Report the malaria status.
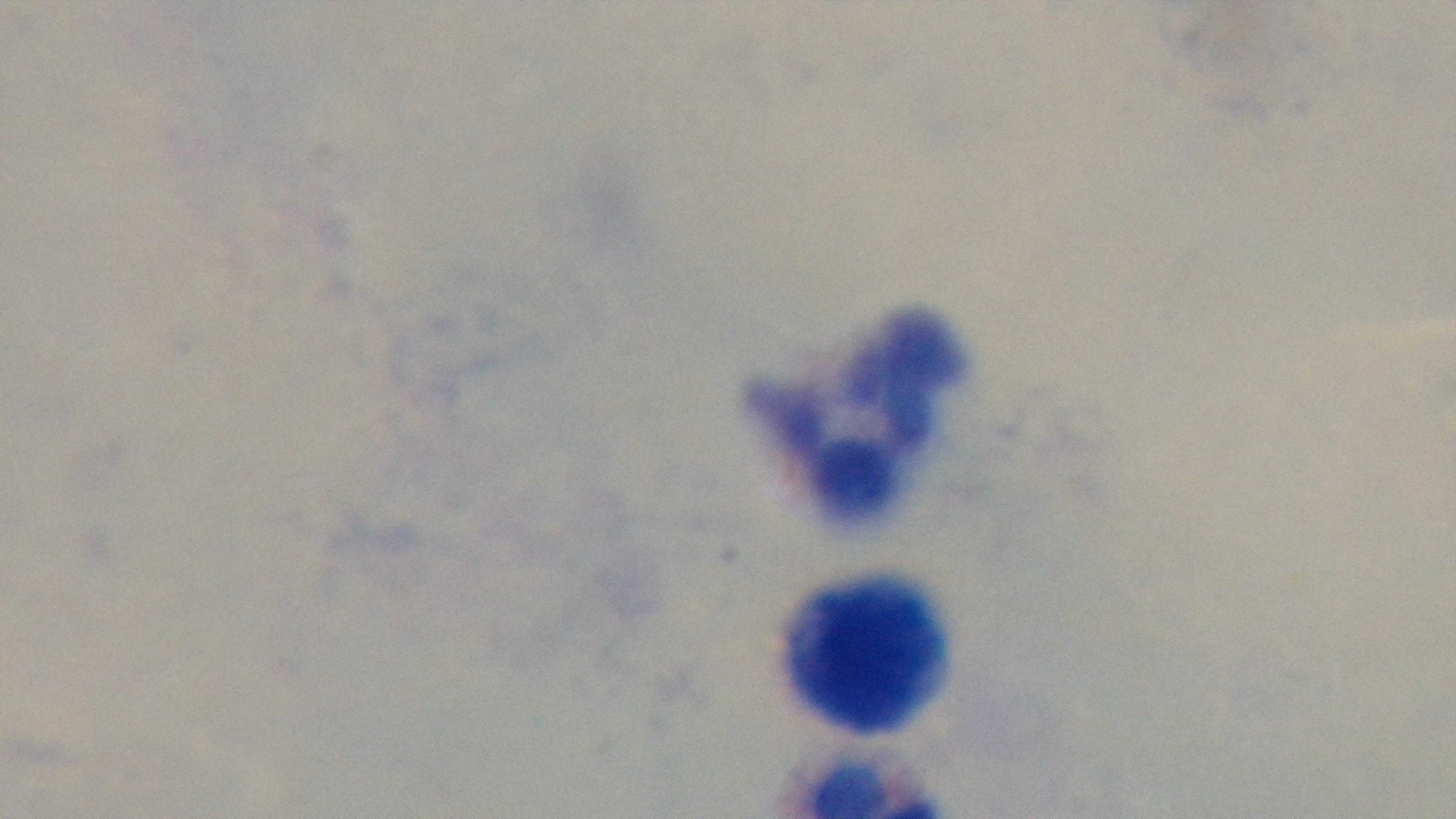

It is uninfected.

Mounted 4K digital camera. One field from the slide. Light microscopy. Giemsa-stained. 100x oil-immersion objective. Preparation: thick.